Report the malaria status of this cell.
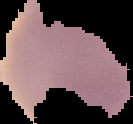
It is uninfected.

From a thin blood film. The area outside the segmented cell region is set to black. Image is 133×124 pixels.